Name the blood parasite species.
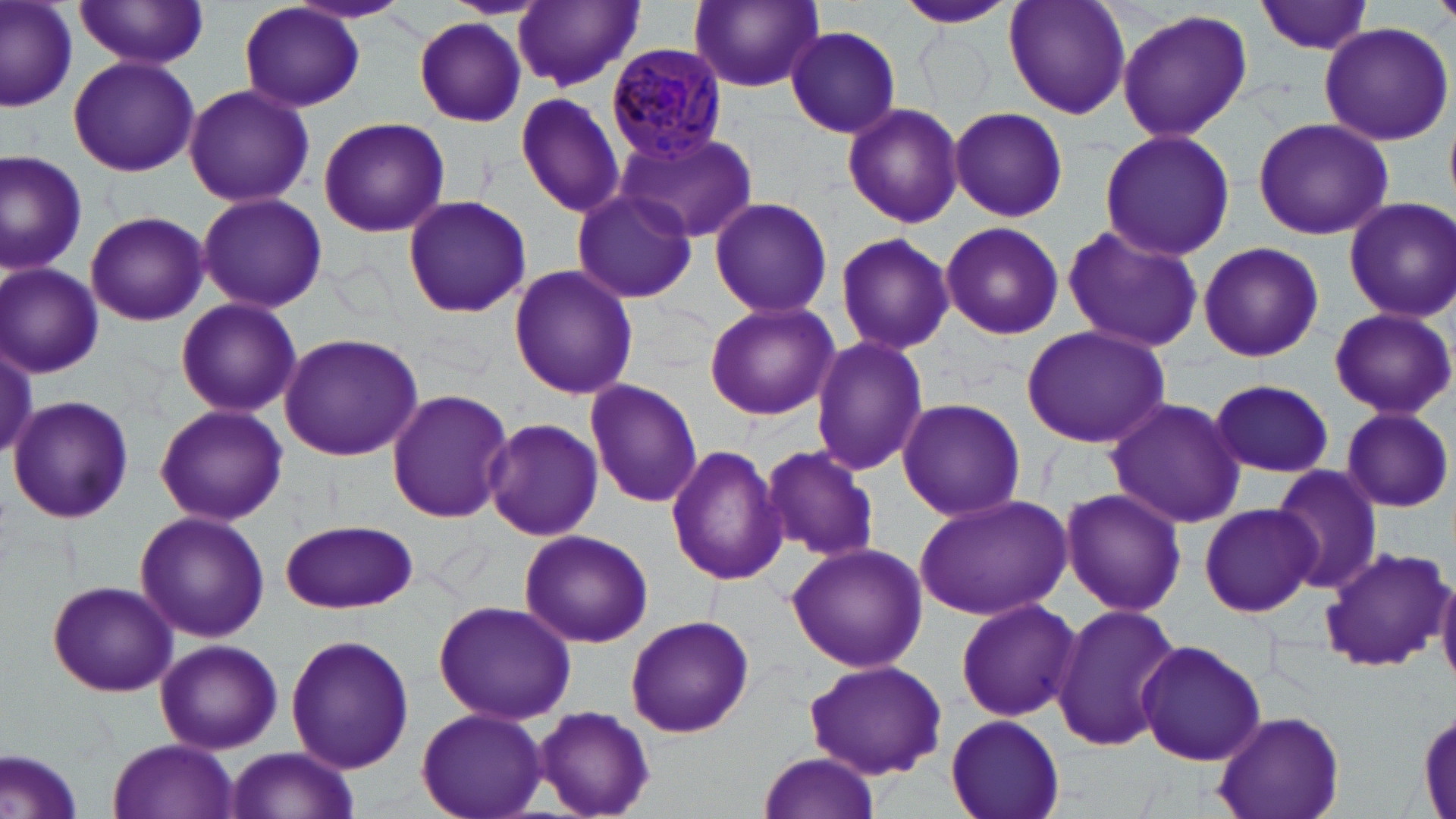

Plasmodium malariae.

Summary:
  - Coordinate format: approximate bounding boxes as (x1,y1)-(x2,y2) corner pairs in pixels
  - Plasmodium malariae-infected red blood cell locations: (606,42)-(727,163)
  - Uninfected red blood cell locations: (1,0)-(81,111), (286,0)-(414,27), (512,0)-(643,91), (685,0)-(827,96), (900,0)-(1016,32), (1001,0)-(1133,119), (75,1)-(210,69), (1255,1)-(1381,55), (239,3)-(366,112), (1114,9)-(1253,142), (414,17)-(527,126), (1319,22)-(1454,146), (785,25)-(903,139), (67,55)-(199,177), (182,83)-(315,209), (512,92)-(629,217), (841,102)-(963,229), (946,106)-(1069,222), (318,116)-(449,239), (1252,118)-(1392,241), (612,129)-(757,241), (1098,129)-(1237,261), (0,149)-(90,275), (568,189)-(697,305), (195,193)-(328,314), (402,193)-(532,319), (708,196)-(833,319), (1343,197)-(1456,321), (537,208)-(668,359), (84,211)-(209,326), (940,220)-(1064,341), (1061,224)-(1205,353), (834,231)-(955,355), (1196,242)-(1324,362), (0,263)-(103,377), (508,263)-(637,400), (174,297)-(301,420), (703,301)-(840,422), (1327,306)-(1454,419), (1021,324)-(1171,450), (278,333)-(424,463), (808,336)-(928,476), (1206,378)-(1338,477), (584,379)-(702,508), (386,387)-(515,524), (7,393)-(134,525), (1104,397)-(1247,529), (897,398)-(1026,523), (154,403)-(288,527), (1340,407)-(1453,512), (482,419)-(605,540), (664,443)-(788,586), (760,443)-(882,565), (1271,463)-(1381,592), (1057,486)-(1188,618), (913,493)-(1071,619), (1199,502)-(1318,617), (134,510)-(269,645), (281,518)-(418,614), (518,530)-(654,648), (786,541)-(927,673), (1319,546)-(1452,672), (1434,571)-(1456,684), (46,579)-(179,698), (954,597)-(1080,722), (430,599)-(575,724), (1052,603)-(1182,753), (624,612)-(754,738), (286,634)-(413,772), (154,639)-(283,754), (1133,640)-(1265,766), (803,660)-(948,779), (415,706)-(548,819), (533,706)-(655,819), (1211,711)-(1345,819), (1417,711)-(1454,818), (943,714)-(1066,819), (105,738)-(241,819), (223,747)-(360,819), (0,748)-(85,819), (754,751)-(885,818)
  - Preparation: thin blood smear
  - Image size: 1456×819 pixels
  - Magnification: 1000x
  - Modality: optical microscopy
  - Stain: May-Grünwald-Giemsa
  - Field of view: one of a larger specimen